Assess the morphology of the erythrocytes.
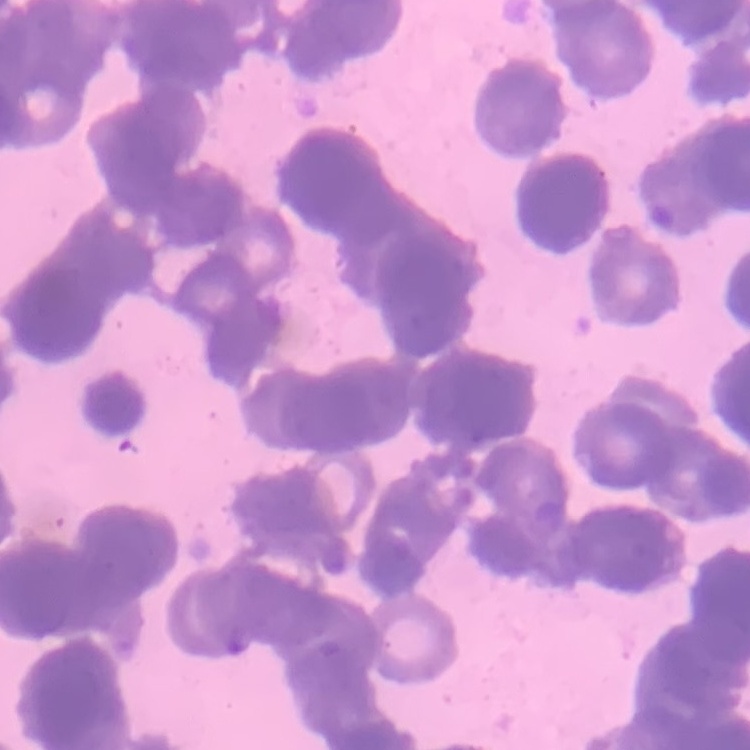

Rouleaux formation.

One tile cut from a larger photomicrograph. Stained with either Field's or Giemsa. Thin blood film.